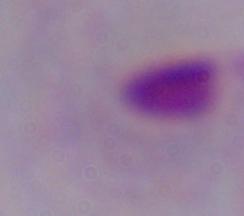
Micrograph. A trichomonad is seen. Captured at 1000x magnification.